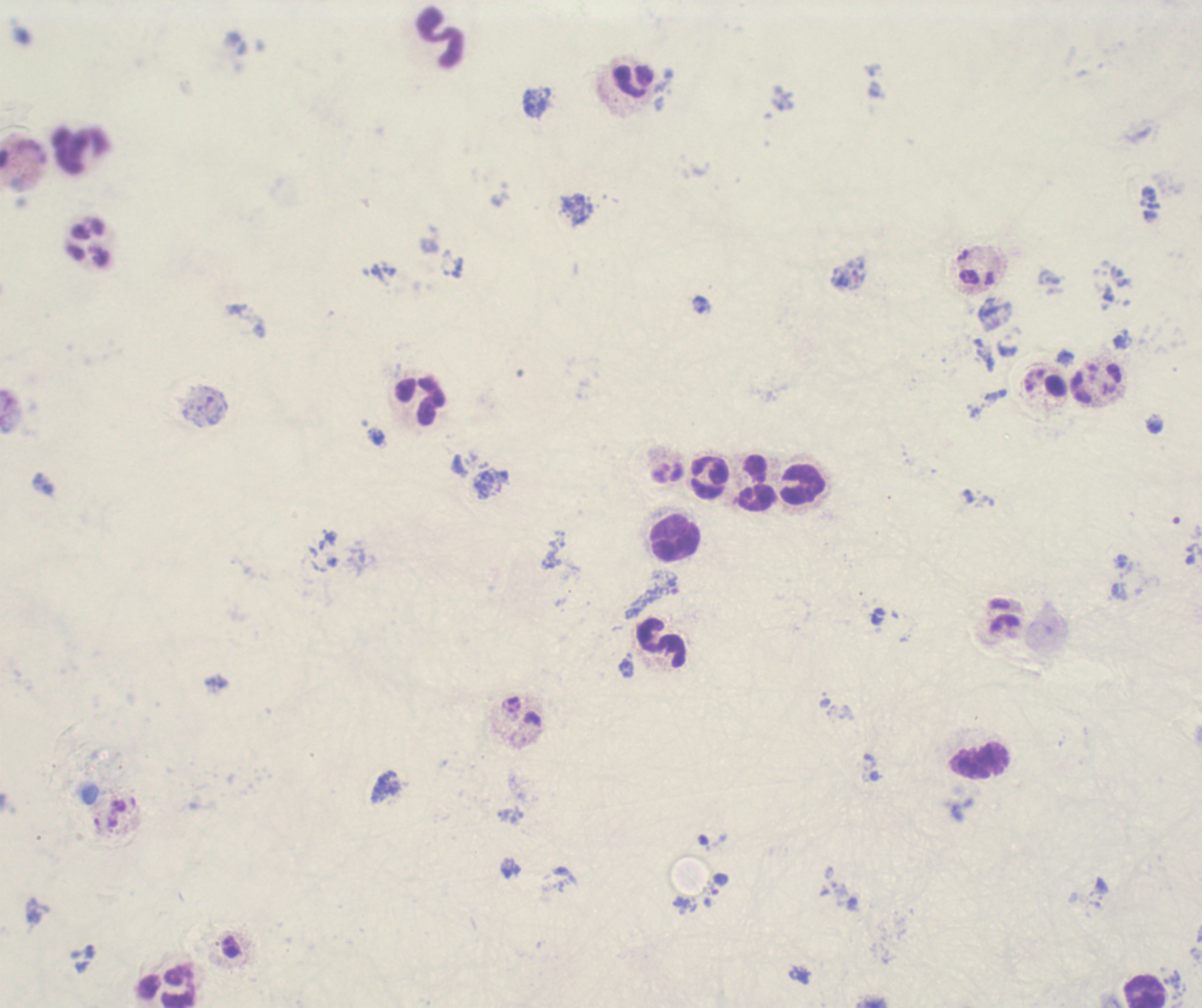 Approximate centers as {x, y} in pixels. Trophozoite locations: {665, 583}, {719, 884}. Leukocyte locations: {440, 37}, {634, 81}, {80, 151}, {421, 401}, {708, 477}, {757, 483}, {802, 483}, {675, 540}, {661, 643}, {980, 761}, {168, 988}, {1146, 990}. Image is 1202×1008 pixels. One field from this slide. Captured at 100x magnification. Romanowsky-stained preparation. Background quality: poor. Result: positive for Plasmodium parasites. Previously used in a real diagnosis. Thick blood smear.